Identify the blood parasite species.
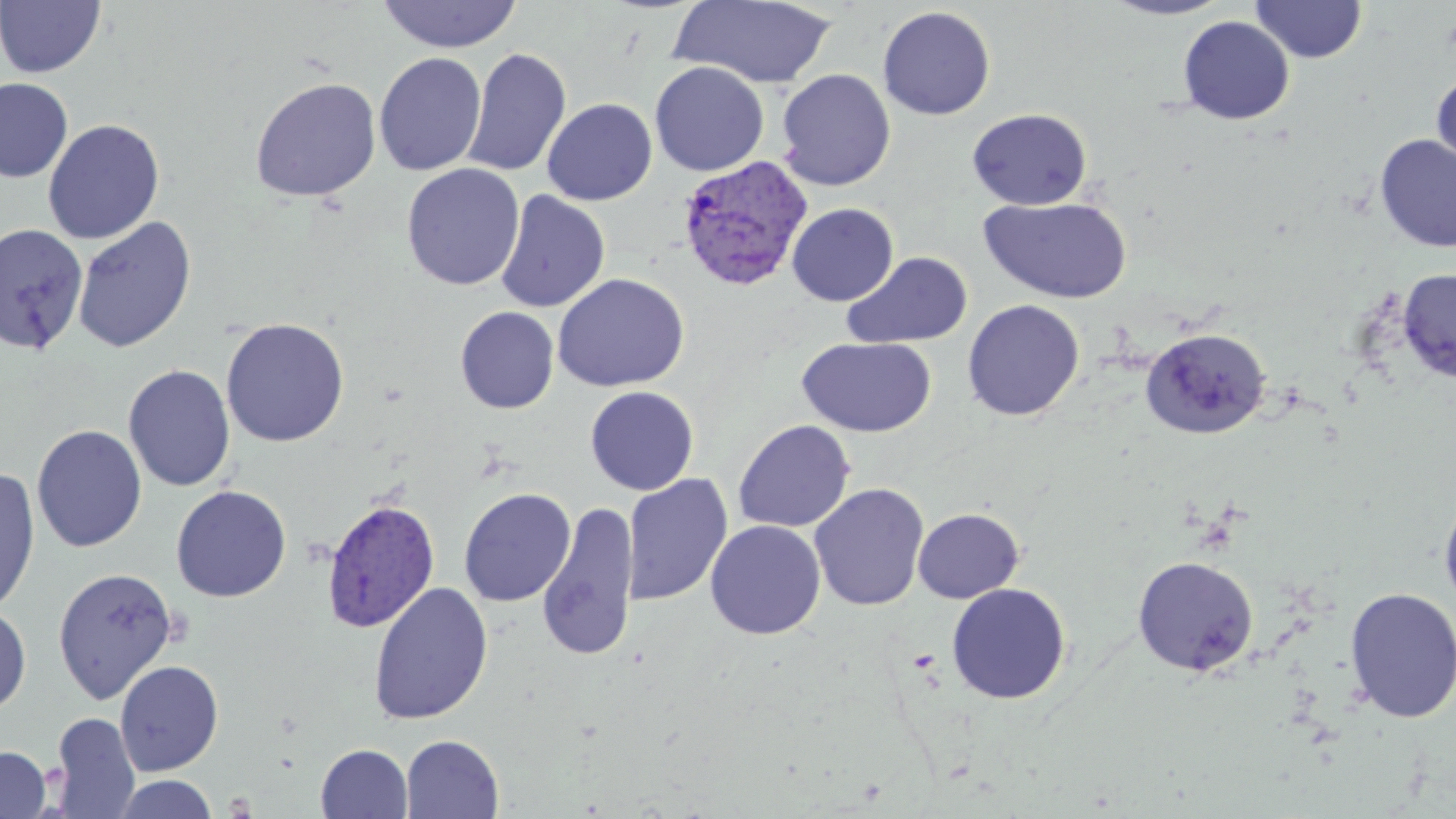
Plasmodium vivax.

Approximate bounding boxes as named x1/y1/x2/y2 corners in pixels. Plasmodium vivax-infected red blood cell locations: (x1=676, y1=155, x2=814, y2=290), (x1=322, y1=498, x2=440, y2=633). Uninfected red blood cell locations: (x1=378, y1=0, x2=522, y2=53), (x1=669, y1=0, x2=838, y2=89), (x1=1100, y1=0, x2=1234, y2=20), (x1=0, y1=1, x2=106, y2=78), (x1=1251, y1=1, x2=1367, y2=63), (x1=878, y1=6, x2=996, y2=120), (x1=1177, y1=16, x2=1294, y2=124), (x1=463, y1=47, x2=571, y2=178), (x1=374, y1=52, x2=487, y2=176), (x1=649, y1=61, x2=770, y2=176), (x1=776, y1=69, x2=896, y2=190), (x1=1431, y1=69, x2=1456, y2=178), (x1=250, y1=77, x2=382, y2=202), (x1=0, y1=78, x2=73, y2=182), (x1=541, y1=98, x2=657, y2=205), (x1=967, y1=108, x2=1092, y2=210), (x1=43, y1=119, x2=164, y2=244), (x1=1374, y1=134, x2=1456, y2=252), (x1=402, y1=163, x2=524, y2=291), (x1=495, y1=191, x2=610, y2=313), (x1=978, y1=195, x2=1133, y2=304), (x1=786, y1=203, x2=899, y2=307), (x1=72, y1=216, x2=197, y2=354), (x1=0, y1=223, x2=89, y2=355), (x1=843, y1=251, x2=972, y2=349), (x1=1397, y1=268, x2=1456, y2=382), (x1=552, y1=272, x2=690, y2=392), (x1=962, y1=299, x2=1085, y2=421), (x1=455, y1=306, x2=559, y2=413), (x1=221, y1=317, x2=349, y2=447), (x1=1140, y1=327, x2=1271, y2=439), (x1=797, y1=337, x2=937, y2=437), (x1=123, y1=365, x2=236, y2=491), (x1=585, y1=386, x2=699, y2=496), (x1=733, y1=420, x2=855, y2=533), (x1=31, y1=424, x2=147, y2=553), (x1=0, y1=466, x2=40, y2=616), (x1=622, y1=474, x2=733, y2=606), (x1=809, y1=483, x2=929, y2=612), (x1=171, y1=485, x2=291, y2=602), (x1=458, y1=488, x2=576, y2=607), (x1=1438, y1=489, x2=1456, y2=615), (x1=536, y1=500, x2=639, y2=662), (x1=913, y1=508, x2=1024, y2=603), (x1=705, y1=520, x2=826, y2=640), (x1=1132, y1=555, x2=1259, y2=676), (x1=53, y1=567, x2=178, y2=703), (x1=946, y1=582, x2=1071, y2=704), (x1=374, y1=585, x2=498, y2=728), (x1=1343, y1=586, x2=1456, y2=724), (x1=0, y1=603, x2=32, y2=716), (x1=114, y1=660, x2=224, y2=776), (x1=50, y1=712, x2=141, y2=818), (x1=400, y1=734, x2=504, y2=818), (x1=316, y1=744, x2=412, y2=818), (x1=0, y1=746, x2=51, y2=819), (x1=110, y1=774, x2=219, y2=818). Thin blood smear. Single field of view. Image is 1456×819 pixels. Optical microscopy. May-Grünwald-Giemsa stain. Captured at 1000x magnification.